Locate platelets.
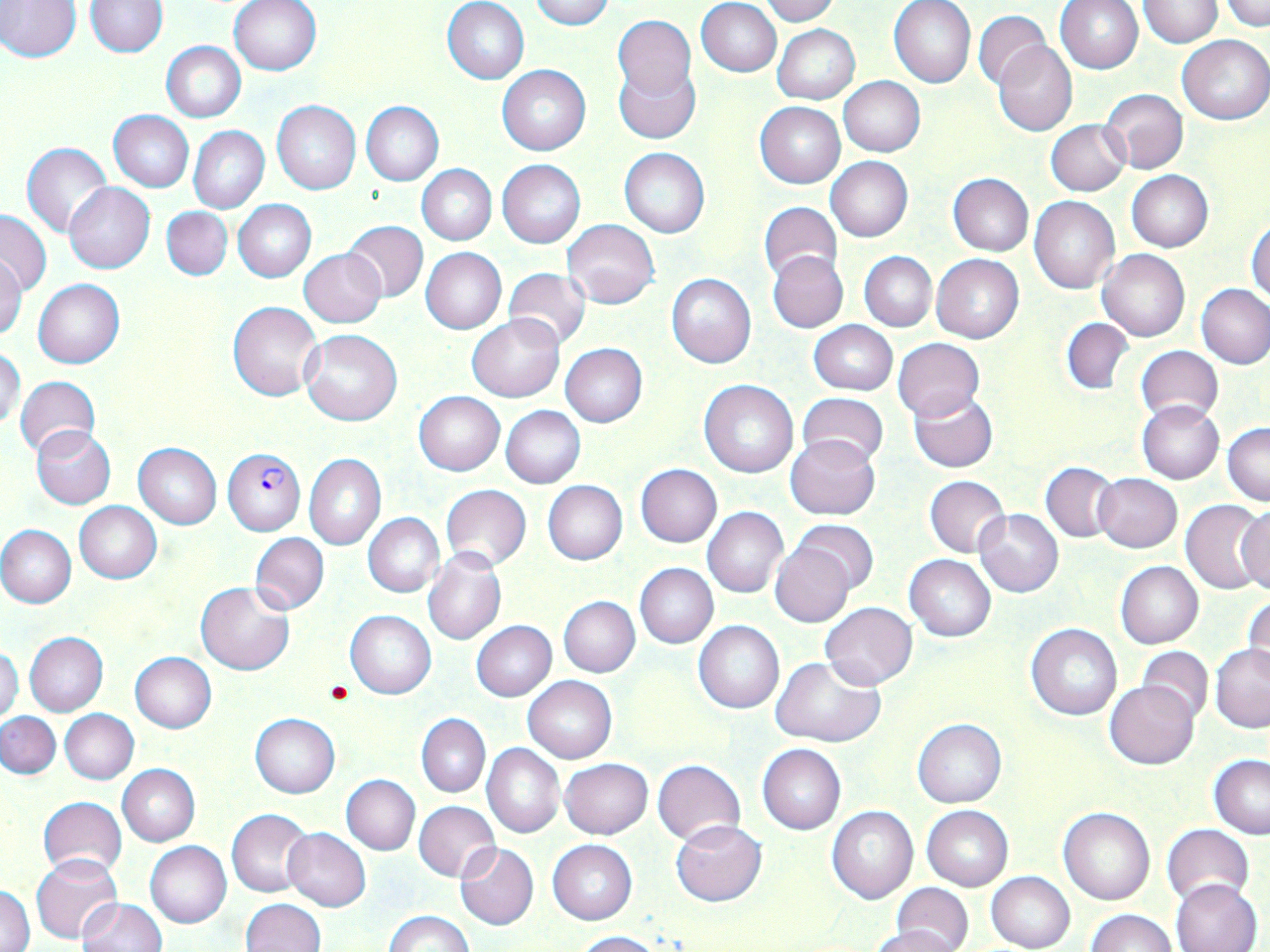

Approximate bounding boxes as [x1, y1, x2, y2] in pixels.
Platelets: [324, 679, 353, 704].

slide-level diagnosis = Plasmodium falciparum
magnification = 1000x
stain = May-Grünwald-Giemsa
image size = 1270×952 pixels
preparation = thin blood film
field of view = one of a larger specimen
Plasmodium falciparum-infected red blood cell locations = approximate bounding boxes as [x1, y1, x2, y2] in pixels: [222, 448, 305, 535]
modality = optical microscopy
uninfected red blood cell locations = approximate bounding boxes as [x1, y1, x2, y2] in pixels: [0, 0, 81, 62], [229, 0, 322, 76], [531, 0, 615, 30], [760, 0, 837, 25], [888, 0, 976, 88], [1056, 0, 1144, 73], [1137, 0, 1223, 47], [1221, 0, 1268, 31], [85, 1, 166, 57], [443, 1, 530, 84], [696, 1, 782, 77], [973, 10, 1049, 90], [612, 15, 695, 103], [773, 24, 860, 103], [1178, 35, 1270, 125], [162, 41, 246, 123], [994, 41, 1077, 136], [613, 61, 699, 145], [497, 63, 590, 154], [839, 76, 925, 157], [1101, 88, 1187, 174], [361, 100, 444, 186], [272, 101, 361, 194], [755, 102, 844, 188], [108, 110, 194, 192], [1045, 119, 1129, 195], [188, 126, 269, 213], [23, 143, 112, 236], [619, 148, 709, 238], [825, 156, 913, 242], [497, 159, 586, 248], [417, 164, 496, 245], [1127, 170, 1213, 252], [947, 173, 1034, 256], [63, 182, 155, 273], [1029, 196, 1118, 294], [232, 199, 315, 282], [758, 201, 841, 282], [162, 206, 232, 280], [0, 209, 52, 295], [562, 219, 660, 307], [1247, 219, 1270, 304], [342, 220, 428, 302], [421, 247, 507, 334], [298, 249, 386, 327], [1098, 249, 1190, 342], [767, 251, 847, 332], [860, 251, 937, 331], [931, 254, 1025, 343], [1, 258, 26, 338], [503, 267, 591, 349], [667, 273, 755, 369], [33, 278, 125, 368], [1196, 284, 1270, 370], [228, 301, 322, 401], [466, 313, 563, 402], [1061, 317, 1134, 394], [809, 320, 897, 396], [301, 328, 402, 426], [893, 338, 984, 420], [561, 343, 647, 428], [1135, 346, 1223, 425], [0, 348, 24, 432], [15, 375, 101, 458], [699, 378, 798, 478], [909, 390, 998, 472], [413, 391, 505, 475], [796, 392, 889, 468], [1137, 400, 1224, 483], [501, 406, 584, 488], [1224, 423, 1270, 506], [32, 427, 115, 508], [784, 434, 880, 521], [134, 443, 222, 529], [304, 454, 385, 550], [1041, 462, 1120, 542], [635, 465, 721, 546], [1094, 472, 1182, 552], [924, 475, 1011, 558], [542, 480, 628, 565], [440, 483, 532, 573], [1180, 499, 1270, 594], [73, 501, 161, 584], [1237, 505, 1270, 595], [702, 506, 788, 597], [974, 508, 1063, 597], [362, 513, 444, 598], [792, 520, 878, 593], [0, 525, 76, 608], [249, 532, 329, 615], [770, 541, 857, 627], [423, 550, 506, 646], [904, 554, 996, 641], [1115, 561, 1203, 648], [636, 563, 717, 648], [196, 582, 294, 675], [1244, 595, 1270, 683], [558, 596, 639, 678], [821, 601, 916, 689], [346, 611, 436, 698], [694, 620, 784, 714], [471, 621, 556, 700], [1026, 622, 1123, 720], [24, 632, 107, 716], [1211, 645, 1270, 731], [0, 646, 23, 726], [1138, 646, 1212, 723], [129, 652, 216, 733], [771, 655, 886, 748], [523, 677, 616, 763], [1104, 680, 1198, 769], [60, 709, 139, 784], [1, 711, 60, 779], [250, 713, 340, 797], [417, 713, 490, 797], [912, 719, 1006, 807], [482, 744, 565, 838], [757, 744, 846, 834], [1209, 756, 1270, 838], [560, 758, 652, 839], [652, 759, 746, 845], [117, 765, 200, 846], [341, 775, 419, 854], [38, 797, 127, 878], [413, 800, 500, 882], [827, 806, 918, 903], [922, 806, 1013, 890], [1059, 806, 1155, 906], [227, 808, 315, 898], [670, 819, 766, 906], [1162, 824, 1254, 908], [283, 829, 370, 911], [548, 840, 637, 924], [145, 841, 231, 928], [455, 843, 539, 930], [30, 854, 123, 945], [986, 871, 1076, 952], [1170, 878, 1262, 951], [892, 883, 973, 952], [1, 884, 34, 951], [78, 898, 167, 952], [240, 899, 325, 952], [1085, 908, 1177, 952], [384, 910, 474, 952], [874, 923, 963, 952], [574, 930, 660, 951]